Point out cells.
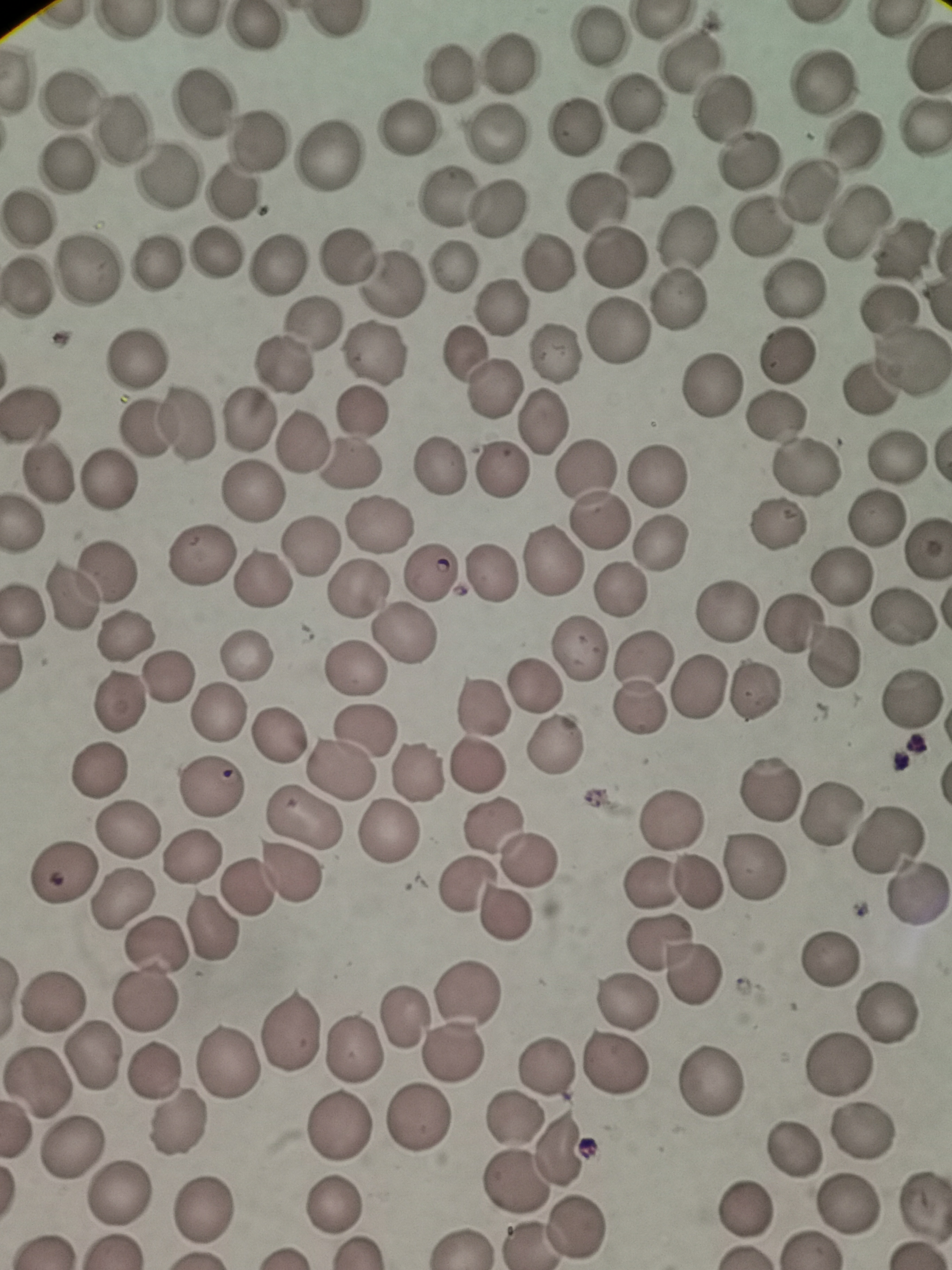

Approximate centers as {x, y} in pixels.
Cells: {250, 29}, {596, 34}, {688, 60}, {508, 63}, {448, 72}, {820, 81}, {69, 97}, {201, 106}, {632, 106}, {722, 108}, {120, 127}, {408, 127}, {576, 128}, {494, 134}, {854, 141}, {257, 142}, {324, 159}, {746, 159}, {71, 165}, {644, 165}, {168, 176}, {810, 191}, {233, 195}, {439, 200}, {599, 204}, {495, 210}, {26, 219}, {855, 223}, {758, 225}, {685, 235}, {902, 246}, {215, 256}, {613, 256}, {157, 257}, {343, 257}, {546, 261}, {451, 264}, {277, 265}, {86, 272}, {388, 284}, {793, 286}, {26, 287}, {680, 299}, {500, 304}, {887, 307}, {310, 323}, {618, 331}, {554, 349}, {465, 352}, {376, 353}, {783, 355}, {135, 360}, {913, 360}, {285, 364}, {711, 384}, {495, 388}, {868, 389}, {361, 412}, {248, 421}, {544, 421}, {777, 421}, {166, 426}, {301, 437}, {897, 454}, {352, 464}, {803, 467}, {436, 468}, {588, 469}, {502, 470}, {655, 478}, {109, 483}, {253, 492}, {872, 519}, {378, 523}, {603, 523}, {776, 526}, {657, 544}, {308, 547}, {927, 549}, {200, 556}, {552, 565}, {108, 570}, {430, 575}, {488, 577}, {840, 577}, {269, 581}, {361, 587}, {620, 590}, {71, 595}, {727, 612}, {902, 615}, {791, 623}, {404, 634}, {124, 635}, {582, 648}, {247, 655}, {830, 657}, {645, 659}, {350, 669}, {165, 677}, {537, 685}, {697, 689}, {752, 693}, {911, 698}, {122, 703}, {480, 707}, {641, 707}, {218, 713}, {365, 731}, {280, 732}, {556, 742}, {480, 765}, {341, 768}, {100, 772}, {416, 772}, {212, 787}, {774, 788}, {830, 810}, {303, 813}, {490, 820}, {673, 820}, {129, 827}, {391, 831}, {885, 842}, {192, 857}, {525, 860}, {752, 867}, {61, 870}, {291, 877}, {466, 885}, {653, 885}, {699, 885}, {247, 888}, {914, 896}, {121, 897}, {502, 911}, {213, 922}, {656, 940}, {160, 945}, {825, 959}, {694, 969}, {469, 994}, {56, 999}, {147, 999}, {628, 1003}, {888, 1013}, {403, 1019}, {292, 1030}, {354, 1048}, {455, 1051}, {94, 1053}, {231, 1063}, {613, 1064}, {841, 1065}, {546, 1066}, {156, 1072}, {712, 1079}, {38, 1082}, {420, 1119}, {511, 1119}, {339, 1125}, {177, 1128}, {72, 1148}, {794, 1148}, {561, 1149}, {515, 1184}, {118, 1191}, {924, 1201}, {338, 1203}, {851, 1204}, {206, 1212}, {744, 1213}, {578, 1227}, {527, 1243}.

Photographed with a smartphone camera at the microscope eyepiece. Thin blood smear. Giemsa-stained preparation. Image is 952×1270 pixels. One field from this slide.